Locate every Plasmodium parasite.
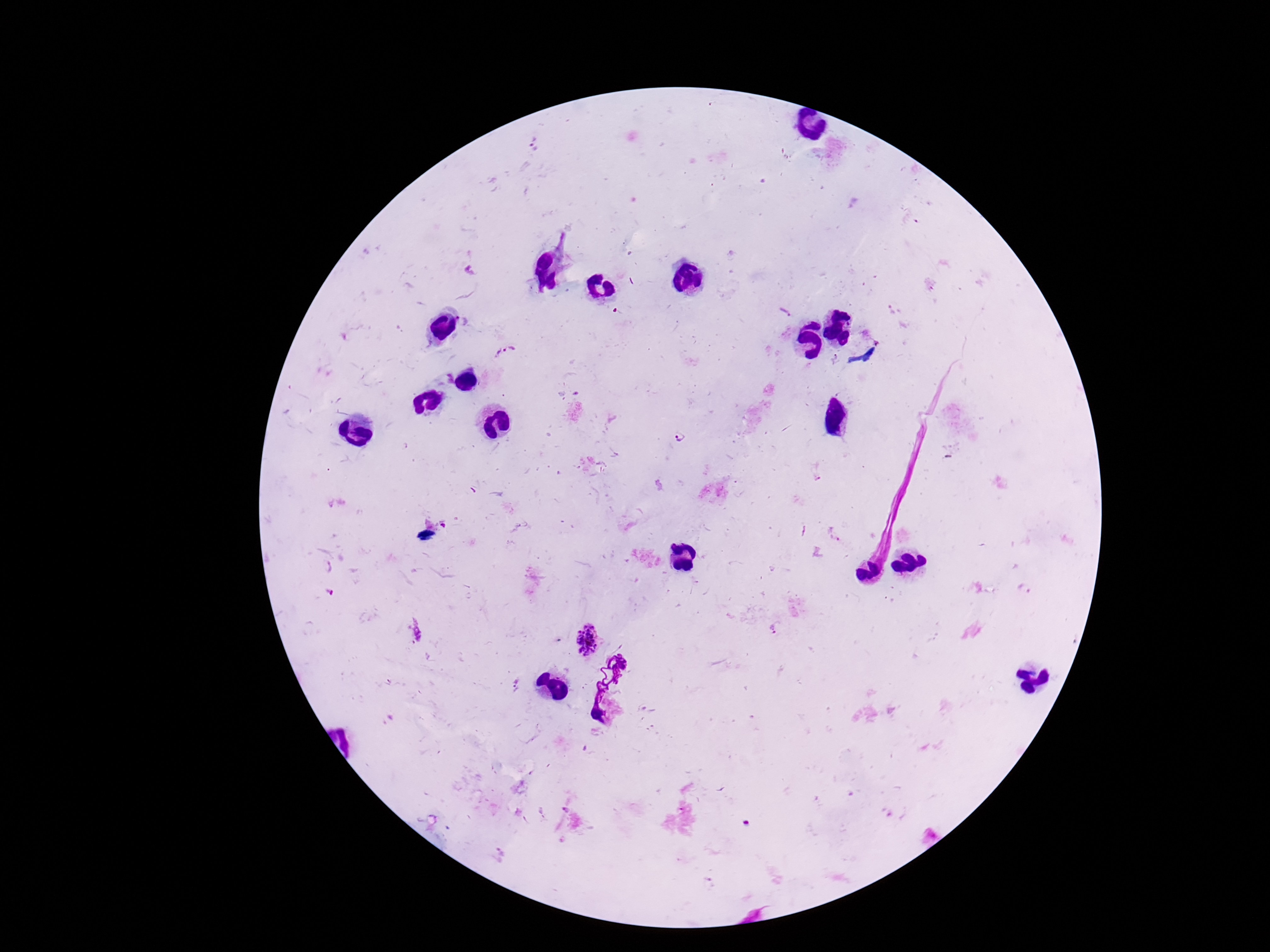

Approximate centers as [x, y] in pixels.
Plasmodium parasites: [532, 143], [785, 312], [507, 353], [836, 362], [679, 437], [833, 536], [586, 640].

patient_malaria_status: positive
field_of_view: single
capture: smartphone camera through the microscope eyepiece
preparation: thick peripheral-blood smear
image_size: 1270×952 pixels
stain: Giemsa
magnification: 100x